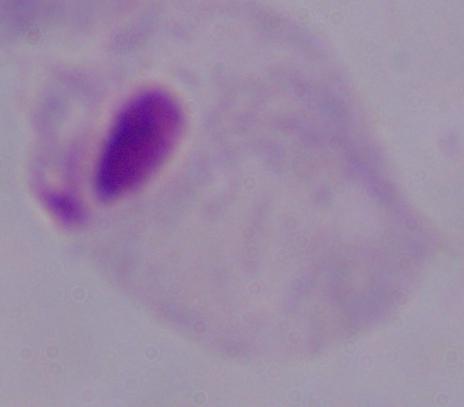
Micrograph. A trichomonad is shown. Captured at 1000x magnification.